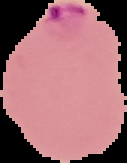

Summary:
  - Preparation: thin blood film
  - Image size: 127×163 pixels
  - Image type: segmented cell region on a black background
  - Malaria status: parasitized